Outline each Plasmodium falciparum-infected red blood cell.
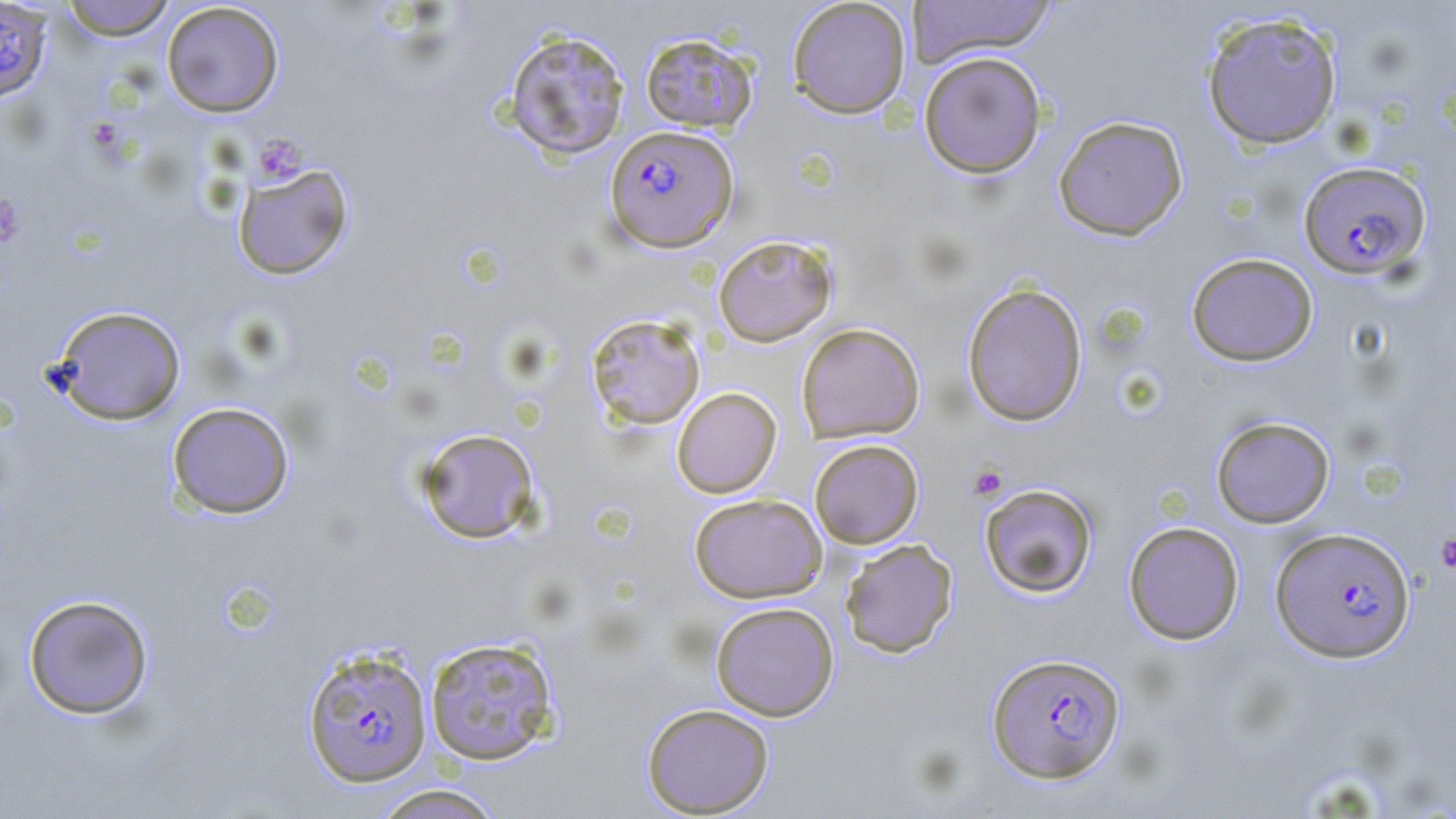
Approximate bounding boxes as [x1, y1, x2, y2] in pixels.
Plasmodium falciparum-infected red blood cells: [0, 1, 53, 104], [604, 125, 738, 252], [1297, 160, 1431, 279], [1270, 526, 1415, 663], [302, 647, 433, 787], [986, 651, 1126, 783].

slide-level diagnosis = Plasmodium falciparum
image size = 1456×819 pixels
preparation = thin blood smear
platelet locations = approximate bounding boxes as [x1, y1, x2, y2] in pixels: [254, 134, 308, 184], [0, 195, 24, 247], [967, 462, 1008, 501], [1435, 531, 1456, 573]
field of view = single
modality = light microscopy
magnification = 1000x
stain = May-Grünwald-Giemsa
uninfected red blood cell locations = approximate bounding boxes as [x1, y1, x2, y2] in pixels: [58, 0, 176, 41], [787, 0, 911, 119], [908, 0, 1056, 66], [161, 2, 284, 118], [1199, 10, 1344, 150], [504, 28, 630, 161], [640, 31, 758, 133], [918, 51, 1047, 179], [1053, 115, 1188, 241], [231, 162, 354, 281], [713, 234, 837, 347], [1186, 252, 1319, 367], [962, 281, 1088, 426], [51, 305, 186, 425], [585, 313, 706, 430], [796, 322, 925, 443], [671, 387, 782, 498], [167, 402, 294, 519], [1211, 415, 1335, 528], [415, 428, 541, 544], [809, 439, 923, 548], [979, 483, 1097, 598], [689, 493, 827, 603], [1123, 521, 1244, 645], [839, 538, 958, 658], [22, 593, 154, 720], [710, 601, 839, 721], [423, 636, 561, 767], [641, 703, 775, 817], [370, 783, 508, 819]